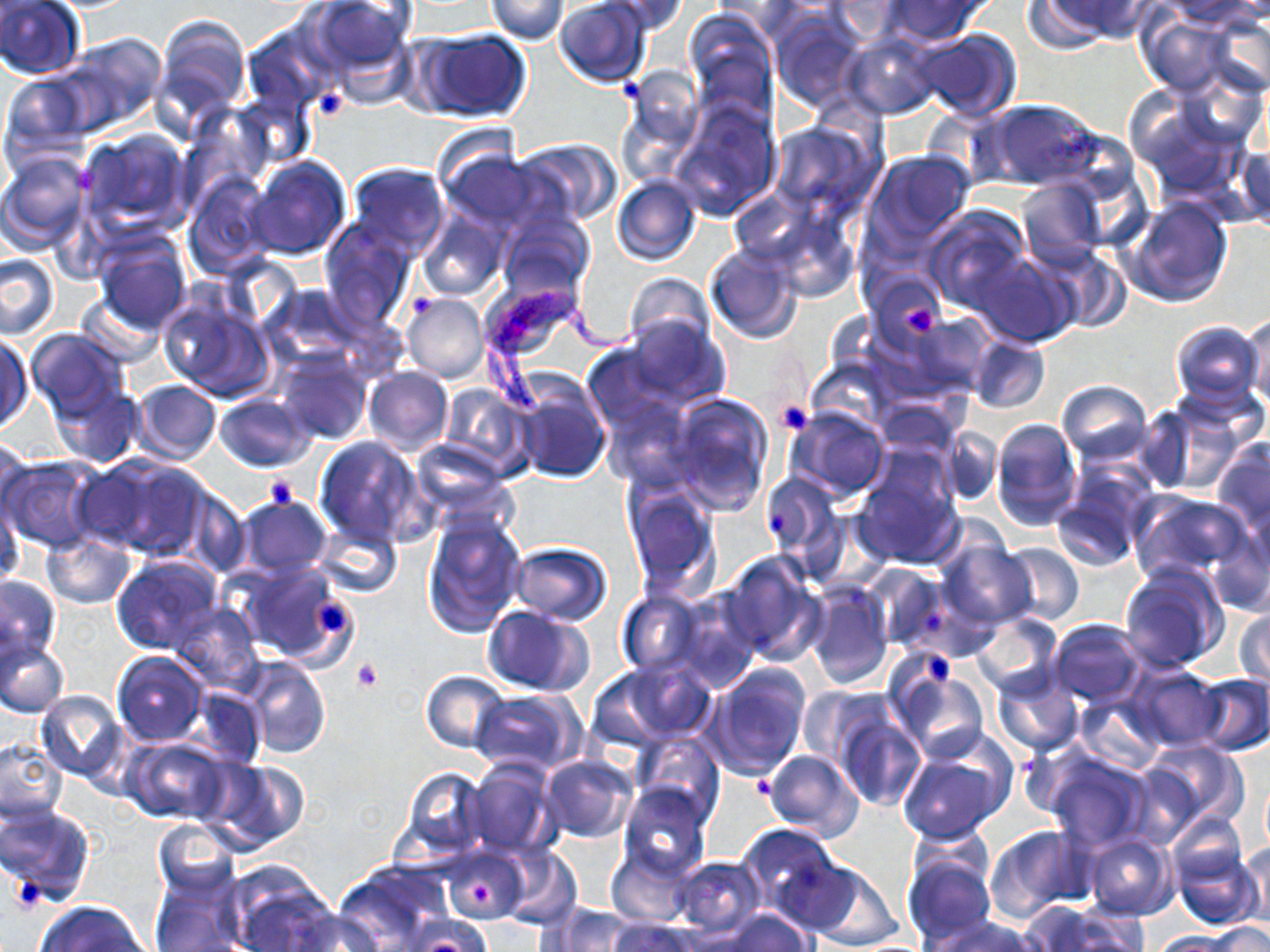

Summary:
  - Coordinate format: approximate bounding boxes as (x1,y1)-(x2,y2) corner pairs in pixels
  - Platelet locations: (617,74)-(644,104), (312,88)-(347,121), (413,295)-(431,316), (902,305)-(936,338), (774,399)-(816,434), (265,476)-(298,510), (764,510)-(789,535), (312,601)-(346,635), (927,650)-(957,689), (352,660)-(383,692), (752,775)-(779,801), (17,878)-(44,906), (469,882)-(493,904)
  - Uninfected red blood cell locations: (308,0)-(419,90), (486,0)-(569,43), (596,0)-(689,35), (1033,0)-(1154,48), (1169,0)-(1266,30), (0,1)-(85,80), (553,1)-(652,87), (881,1)-(986,41), (683,9)-(779,124), (772,13)-(864,112), (1138,13)-(1239,99), (1211,15)-(1270,96), (152,16)-(249,130), (412,27)-(532,124), (909,28)-(1021,122), (843,34)-(938,120), (48,35)-(166,139), (620,66)-(703,167), (1124,90)-(1246,197), (983,98)-(1104,191), (671,100)-(782,220), (767,121)-(878,218), (79,131)-(191,235), (515,138)-(623,227), (1235,141)-(1269,231), (440,144)-(550,232), (863,150)-(976,252), (0,151)-(90,251), (248,156)-(351,260), (346,163)-(448,257), (184,174)-(271,277), (612,174)-(702,267), (1016,177)-(1107,270), (1123,196)-(1232,307), (924,204)-(1032,311), (418,211)-(505,300), (499,214)-(593,297), (320,221)-(416,329), (91,233)-(192,335), (705,244)-(804,344), (1042,249)-(1133,329), (972,251)-(1077,348), (0,253)-(59,338), (865,267)-(951,352), (624,273)-(715,353), (263,285)-(366,366), (481,285)-(574,365), (158,289)-(276,403), (76,293)-(164,367), (401,294)-(489,384), (896,311)-(993,398), (1243,311)-(1270,406), (624,316)-(729,409), (1170,320)-(1264,408), (26,329)-(131,421), (966,335)-(1050,414), (0,336)-(32,434), (275,351)-(371,445), (362,366)-(453,456), (130,379)-(221,465), (49,380)-(143,469), (1056,380)-(1153,465), (512,381)-(610,484), (439,385)-(531,478), (215,393)-(315,472), (670,395)-(771,513), (871,397)-(959,455), (601,398)-(694,489), (1140,398)-(1248,494), (786,408)-(889,503), (991,418)-(1082,530), (939,427)-(1001,505), (313,436)-(428,548), (0,437)-(33,528), (408,440)-(516,523), (1211,440)-(1270,533), (852,452)-(965,570), (3,456)-(104,553), (80,456)-(212,561), (759,471)-(843,569), (1051,477)-(1146,571), (624,485)-(720,599), (1129,493)-(1252,584), (233,496)-(333,579), (1,504)-(23,589), (422,513)-(527,637), (1210,519)-(1270,616), (315,523)-(402,598), (40,532)-(135,609), (936,539)-(1035,631), (508,542)-(611,626), (999,543)-(1084,627), (721,549)-(826,665), (110,554)-(224,658), (861,562)-(948,651), (235,563)-(354,666), (1119,563)-(1229,672), (0,574)-(61,666), (803,581)-(894,692), (616,590)-(705,678), (675,591)-(762,693), (168,602)-(263,692), (482,606)-(594,697), (1235,607)-(1270,687), (972,612)-(1064,701), (1047,618)-(1146,707), (1,636)-(70,719), (111,651)-(210,746), (244,657)-(330,759), (602,658)-(720,744), (699,662)-(811,780), (1125,663)-(1226,752), (421,671)-(510,753), (894,672)-(987,762), (990,672)-(1083,758), (1191,675)-(1269,755), (797,686)-(891,768), (188,687)-(266,768), (470,689)-(583,774), (35,690)-(128,781), (1075,696)-(1165,772), (833,709)-(926,814), (632,732)-(723,823), (124,737)-(230,824), (0,738)-(66,825), (1139,741)-(1245,834), (896,748)-(1008,844), (764,749)-(863,840), (1039,749)-(1153,851), (539,755)-(638,842), (199,756)-(310,853), (466,760)-(556,857), (400,766)-(489,861), (1261,776)-(1270,853), (618,784)-(711,881), (0,805)-(96,908), (1165,811)-(1247,889), (152,820)-(240,900), (735,824)-(842,919), (986,825)-(1094,921), (1080,832)-(1178,920), (1171,841)-(1262,932), (1239,843)-(1270,930), (499,847)-(582,929), (444,848)-(527,923), (606,849)-(695,926), (669,855)-(766,937), (901,855)-(995,949), (768,856)-(866,935), (225,862)-(335,952), (796,862)-(901,949), (330,865)-(447,948), (151,871)-(243,952), (35,901)-(150,952), (1016,901)-(1132,952), (549,904)-(634,952), (279,908)-(386,952), (719,909)-(810,952), (399,915)-(495,951), (924,915)-(1040,952), (606,918)-(696,952), (1207,922)-(1270,952), (1152,931)-(1240,951)
  - Trypanosoma brucei locations: (477,288)-(663,421)
  - Slide-level diagnosis: Trypanosoma brucei
  - Modality: light microscopy
  - Stain: May-Grünwald-Giemsa
  - Field of view: single
  - Image size: 1270×952 pixels
  - Preparation: thin blood smear
  - Magnification: 1000x